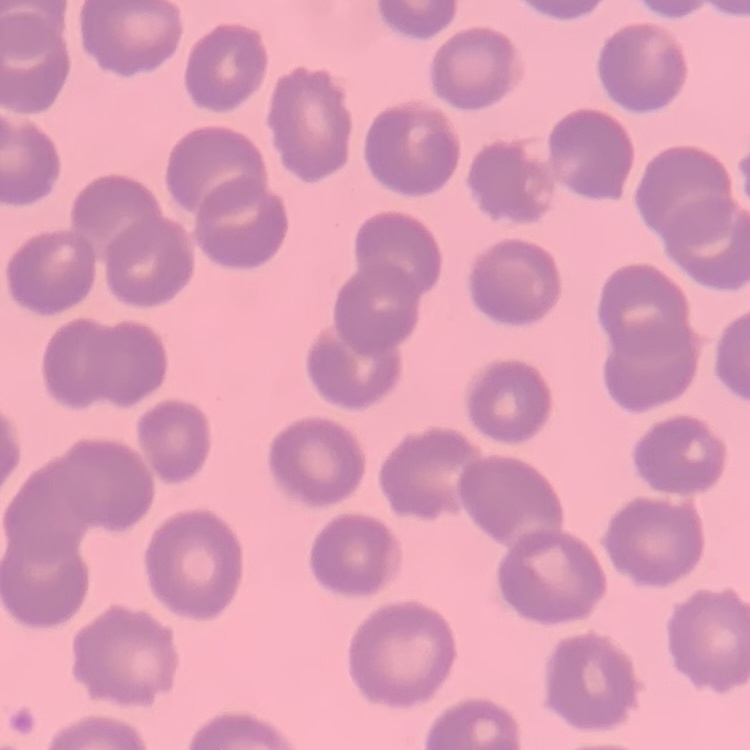 The red blood cells exhibit no rouleaux formation. Square crop of a larger photomicrograph. Field's or Giemsa stain. Thin blood film.